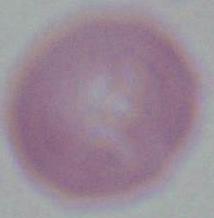

Summary:
  - Modality: photomicrograph
  - Identification: red blood cell
  - Magnification: 1000x